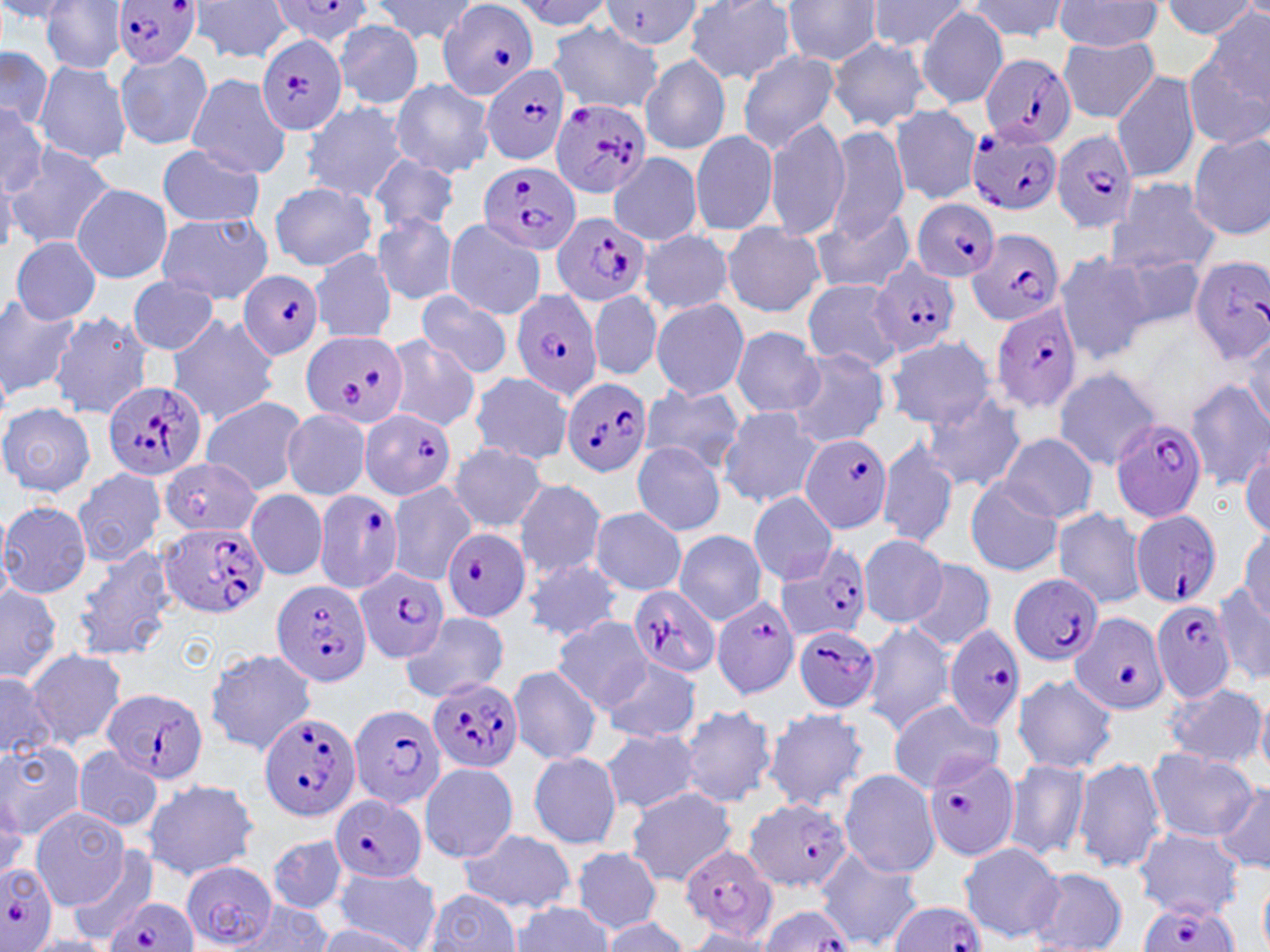
Summary:
  - Coordinate format: approximate bounding boxes as [x1, y1, x2, y2] in pixels
  - Uninfected red blood cell locations (subset): [370, 0, 478, 46], [508, 0, 612, 30], [780, 0, 886, 66], [868, 0, 971, 51], [1160, 0, 1258, 39], [0, 1, 77, 28], [41, 1, 129, 74], [189, 1, 293, 64], [602, 1, 704, 50], [682, 1, 798, 85], [964, 1, 1072, 43], [1055, 1, 1164, 50], [916, 6, 1008, 109], [1205, 8, 1269, 100], [333, 20, 424, 110], [547, 23, 664, 113], [1057, 35, 1159, 123], [827, 36, 930, 133], [0, 45, 56, 132], [114, 49, 214, 152], [735, 51, 841, 155], [1181, 53, 1270, 152], [641, 55, 732, 155], [33, 60, 132, 167], [1111, 69, 1202, 183], [185, 72, 293, 179], [388, 79, 496, 178], [300, 100, 409, 203], [0, 102, 49, 198], [889, 104, 981, 203], [765, 116, 850, 241], [825, 126, 910, 242], [690, 129, 780, 237], [1187, 133, 1270, 239], [6, 146, 117, 251], [156, 146, 265, 229], [611, 148, 703, 242], [369, 155, 462, 233], [0, 166, 18, 257], [1106, 180, 1220, 276], [268, 182, 377, 272], [72, 183, 171, 284], [811, 208, 916, 296], [156, 211, 273, 304], [372, 213, 461, 305], [443, 219, 547, 319], [721, 222, 825, 317], [638, 228, 734, 315], [10, 237, 101, 324], [310, 248, 398, 345], [1052, 251, 1150, 365], [1107, 251, 1211, 336], [126, 276, 223, 355], [803, 279, 904, 371], [589, 288, 661, 382], [417, 292, 514, 379], [0, 293, 79, 400], [650, 298, 749, 400], [49, 310, 154, 421], [165, 313, 281, 427], [1241, 323, 1270, 432], [730, 327, 825, 417], [383, 336, 482, 434], [884, 337, 996, 428], [786, 349, 891, 448], [1052, 367, 1161, 470], [467, 371, 575, 463], [1185, 379, 1270, 489], [638, 383, 745, 474], [917, 391, 1027, 494], [198, 396, 308, 496], [0, 404, 95, 496], [717, 405, 821, 508], [280, 408, 373, 500], [877, 431, 959, 550], [996, 434, 1099, 524], [630, 441, 726, 537], [1239, 441, 1269, 540], [449, 443, 550, 534], [160, 458, 258, 541], [71, 468, 166, 568], [512, 478, 606, 579], [965, 479, 1064, 578], [246, 489, 328, 580], [746, 492, 839, 584], [0, 501, 92, 598], [589, 507, 687, 596], [1051, 507, 1147, 609], [1236, 529, 1269, 626], [675, 531, 768, 624], [857, 534, 950, 627], [67, 544, 177, 662], [521, 557, 625, 644], [906, 560, 995, 651], [0, 581, 63, 682], [1213, 582, 1270, 685], [400, 611, 510, 704], [550, 617, 653, 713], [860, 622, 955, 735], [24, 648, 127, 747], [202, 648, 318, 755], [599, 659, 703, 743], [506, 664, 602, 765], [0, 672, 57, 761], [1012, 672, 1117, 774], [1161, 683, 1267, 769], [1254, 694, 1270, 778], [887, 699, 1004, 794], [674, 703, 776, 808], [763, 706, 868, 811], [600, 728, 703, 814], [0, 741, 86, 837], [71, 748, 165, 832], [1145, 748, 1255, 841], [527, 753, 625, 851], [1003, 757, 1093, 862], [1074, 757, 1167, 874], [419, 762, 517, 862], [838, 769, 941, 877], [140, 778, 261, 881], [1214, 781, 1270, 875], [625, 787, 736, 887], [30, 808, 131, 907], [456, 828, 577, 914], [1136, 829, 1243, 918], [268, 835, 348, 913], [958, 841, 1064, 943], [68, 846, 159, 946], [571, 848, 663, 933], [814, 848, 923, 950], [332, 866, 441, 951], [1024, 867, 1129, 952], [1258, 868, 1270, 952], [423, 887, 525, 952], [231, 902, 335, 950], [510, 903, 614, 952], [599, 916, 692, 951], [313, 925, 420, 951], [679, 928, 777, 951], [24, 934, 115, 952]
  - Plasmodium falciparum-infected red blood cell locations (subset): [112, 0, 203, 71], [273, 1, 378, 46], [436, 1, 540, 100], [256, 32, 349, 138], [980, 54, 1076, 147], [479, 64, 571, 166], [550, 98, 650, 201], [966, 125, 1061, 217], [1050, 129, 1140, 236], [478, 163, 580, 254], [911, 200, 1000, 281], [549, 213, 652, 307], [965, 227, 1065, 328], [1187, 255, 1270, 365], [870, 259, 961, 358], [238, 270, 324, 359], [509, 287, 603, 402], [990, 301, 1083, 415], [301, 331, 409, 429], [562, 377, 652, 477], [100, 380, 208, 486], [360, 407, 456, 500], [1110, 416, 1209, 523], [799, 435, 893, 536], [313, 488, 403, 592], [1131, 510, 1224, 609], [158, 522, 267, 617], [442, 528, 529, 623], [776, 544, 874, 644], [356, 564, 450, 664], [1009, 575, 1102, 667], [270, 579, 372, 686], [626, 585, 720, 679], [711, 595, 801, 697], [1148, 599, 1238, 703], [1070, 612, 1169, 716], [943, 623, 1026, 731], [793, 625, 881, 712], [428, 676, 523, 773], [105, 688, 208, 787], [346, 703, 445, 810], [257, 711, 359, 823], [924, 748, 1023, 867], [329, 795, 427, 882], [745, 796, 853, 894], [680, 844, 779, 944], [180, 860, 278, 949], [0, 861, 58, 951], [106, 897, 196, 952], [886, 902, 987, 952], [1135, 903, 1237, 952], [756, 904, 856, 952]
  - Slide-level diagnosis: Plasmodium falciparum
  - Field of view: one of a larger specimen
  - Modality: light microscopy
  - Magnification: 1000x
  - Image size: 1270×952 pixels
  - Stain: May-Grünwald-Giemsa
  - Preparation: thin blood smear